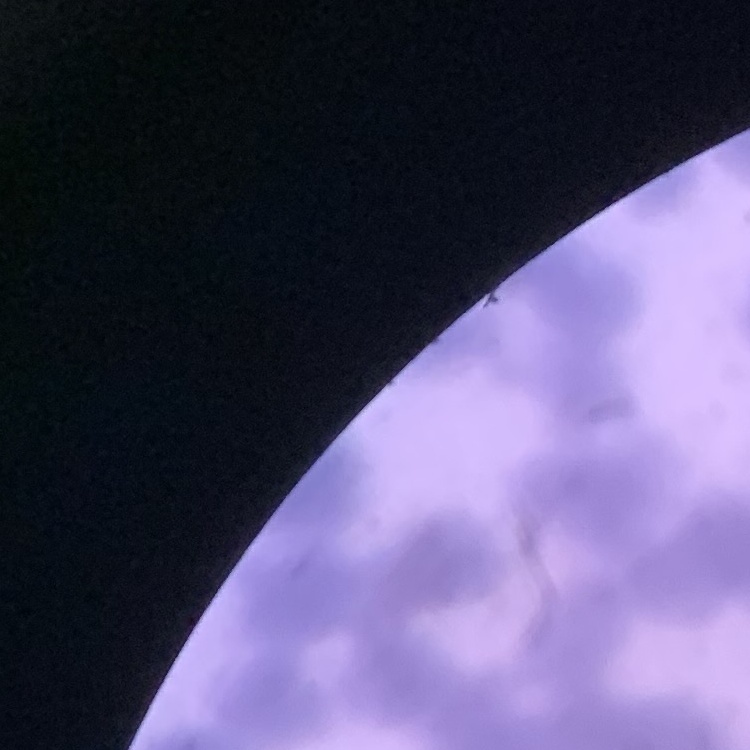

The red blood cells show rouleaux formation. Field's or Giemsa stain. One tile cut from a larger photomicrograph. Thin blood film.